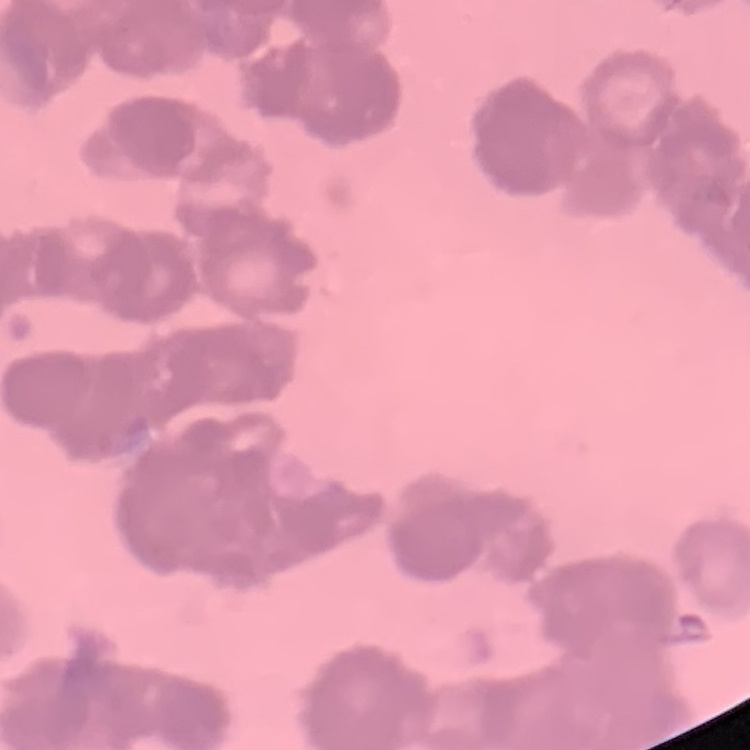
The red blood cells show rouleaux formation. Thin blood smear. Field's or Giemsa stain. Square crop of a larger photomicrograph.